Assess this cell for malaria.
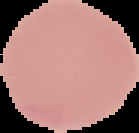

Uninfected.

Image is 139×133 pixels. The area outside the segmented cell region is set to black. From a thin blood smear.